Assess the morphology of the erythrocytes.
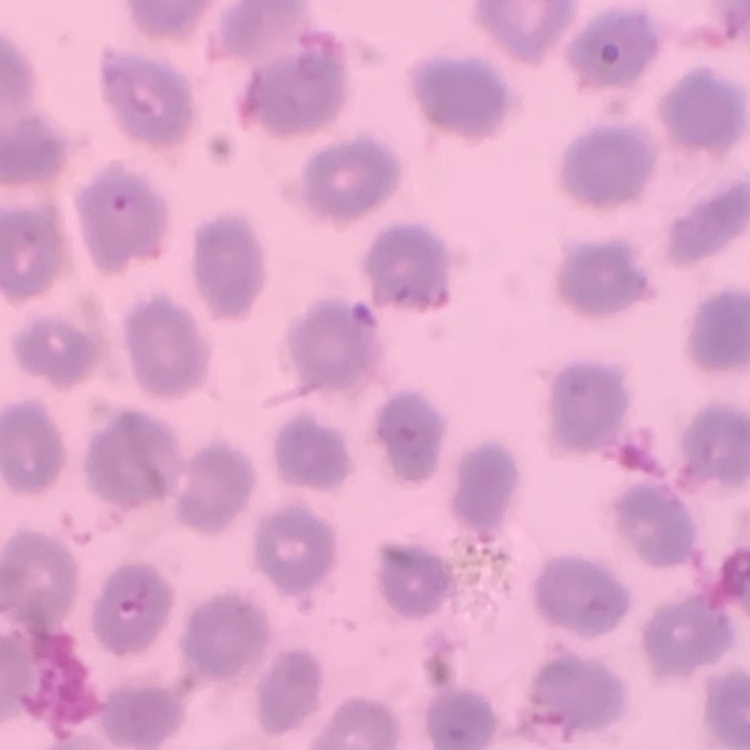
They show no rouleaux formation.

Summary:
  - Preparation: thin blood smear
  - Image type: square crop of a larger photomicrograph
  - Stain: Field's or Giemsa